Assess the morphology of the erythrocytes.
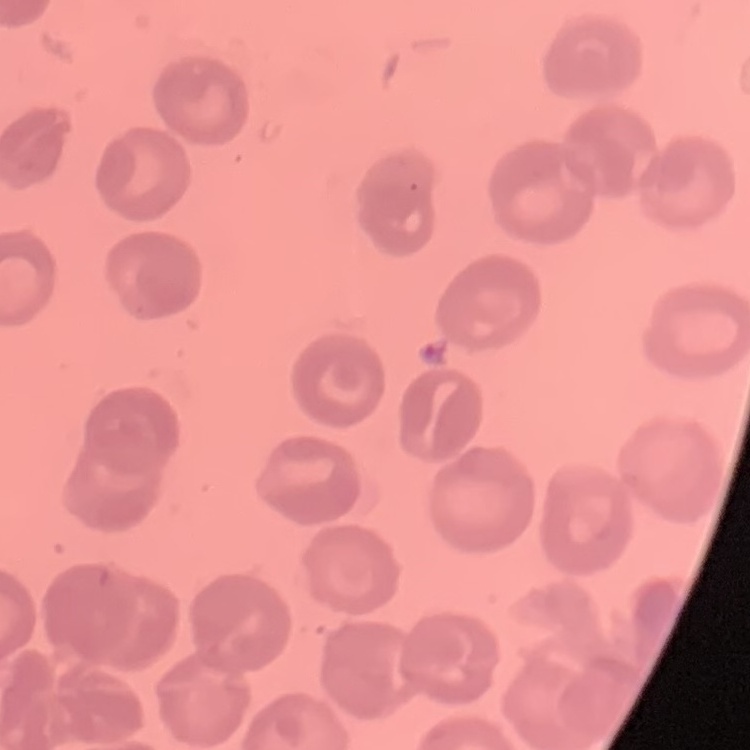
They show no rouleaux formation.

Thin blood film. Field's or Giemsa stain. Square crop of a larger photomicrograph.